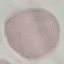

malaria status = uninfected
capture = smartphone camera at the microscope eyepiece
preparation = thin smear
image type = automatically extracted cell patch, resized to 64 × 64 pixels
stain = Giemsa